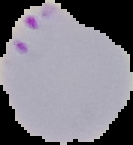
Summary:
  - Image type: cell region segmented out of the field of view; surrounding area masked to black
  - Image size: 133×145 pixels
  - Result: malaria parasites identified
  - Preparation: thin blood film